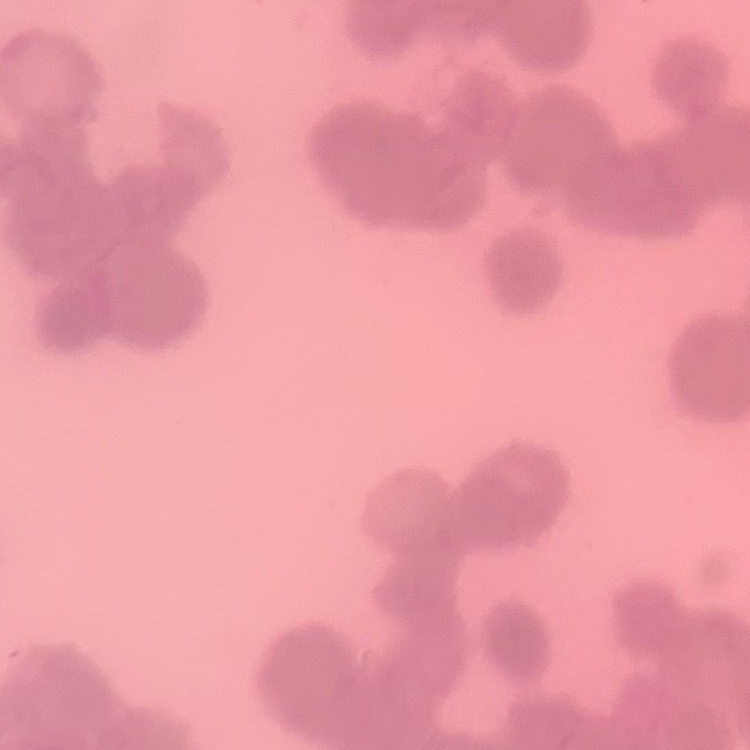
{
  "red_blood_cell_morphology": "rouleaux formation",
  "preparation": "thin peripheral smear",
  "stain": "Field's or Giemsa",
  "image_type": "one tile cut from a larger photomicrograph"
}